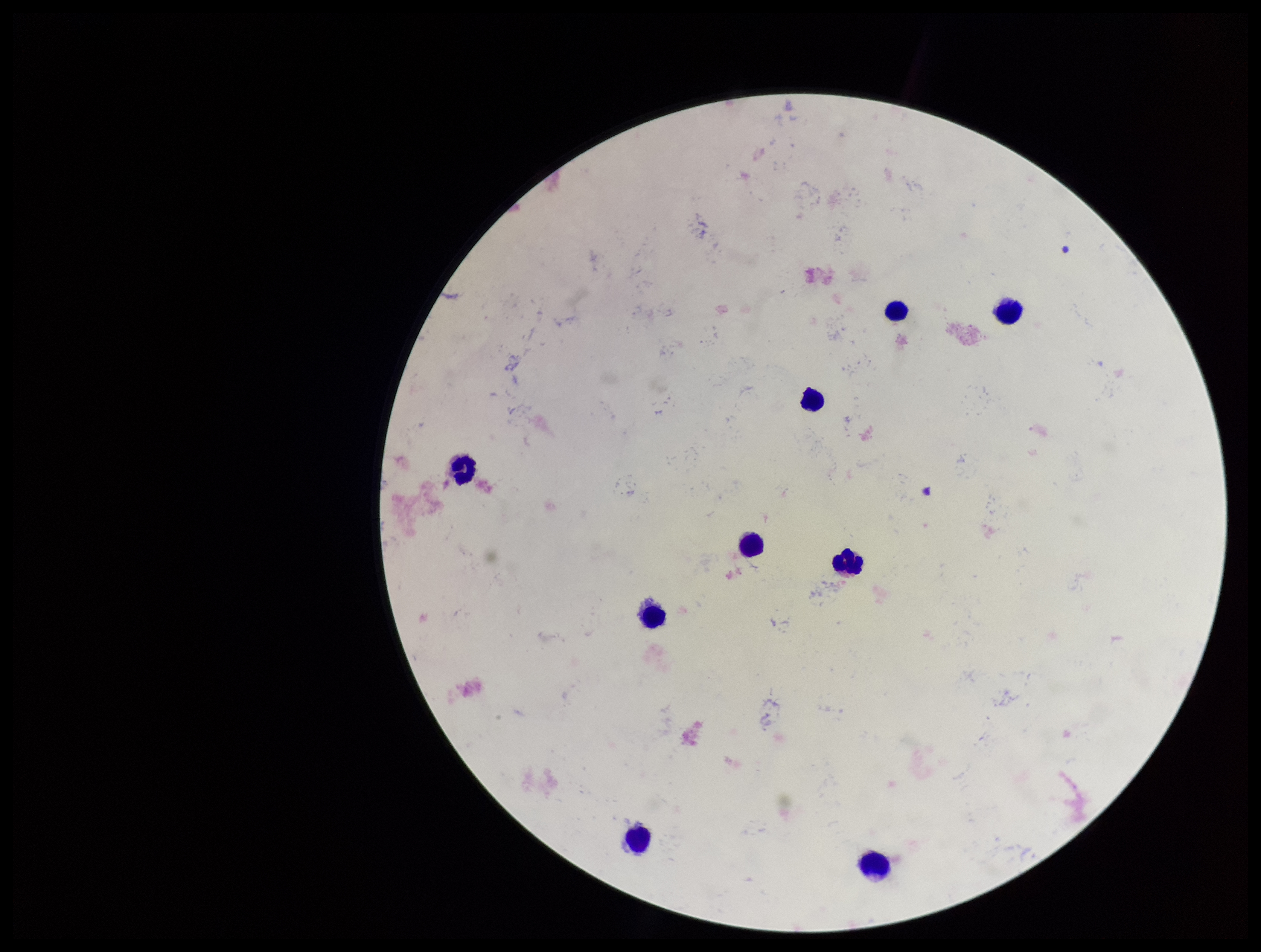
Single field of view. Preparation: thick. Image is 1261×952 pixels. Plasmodium parasites: none identified. Patient malaria status: negative. Photographed through the microscope eyepiece with a smartphone camera. Giemsa stain. Leukocyte count: 9. Parasite count: 0.